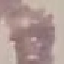

malaria status = uninfected
capture = smartphone camera at the microscope eyepiece
preparation = thin blood smear
image type = automatically extracted cell patch, resized to 64 × 64 pixels
stain = Giemsa